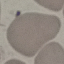
Summary:
  - Malaria status: uninfected
  - Capture: smartphone camera at the microscope eyepiece
  - Image type: automatically extracted cell patch, resized to 64 × 64 pixels
  - Preparation: thin blood film
  - Stain: Giemsa